Draw a bounding box around every leukocyte (white blood cell).
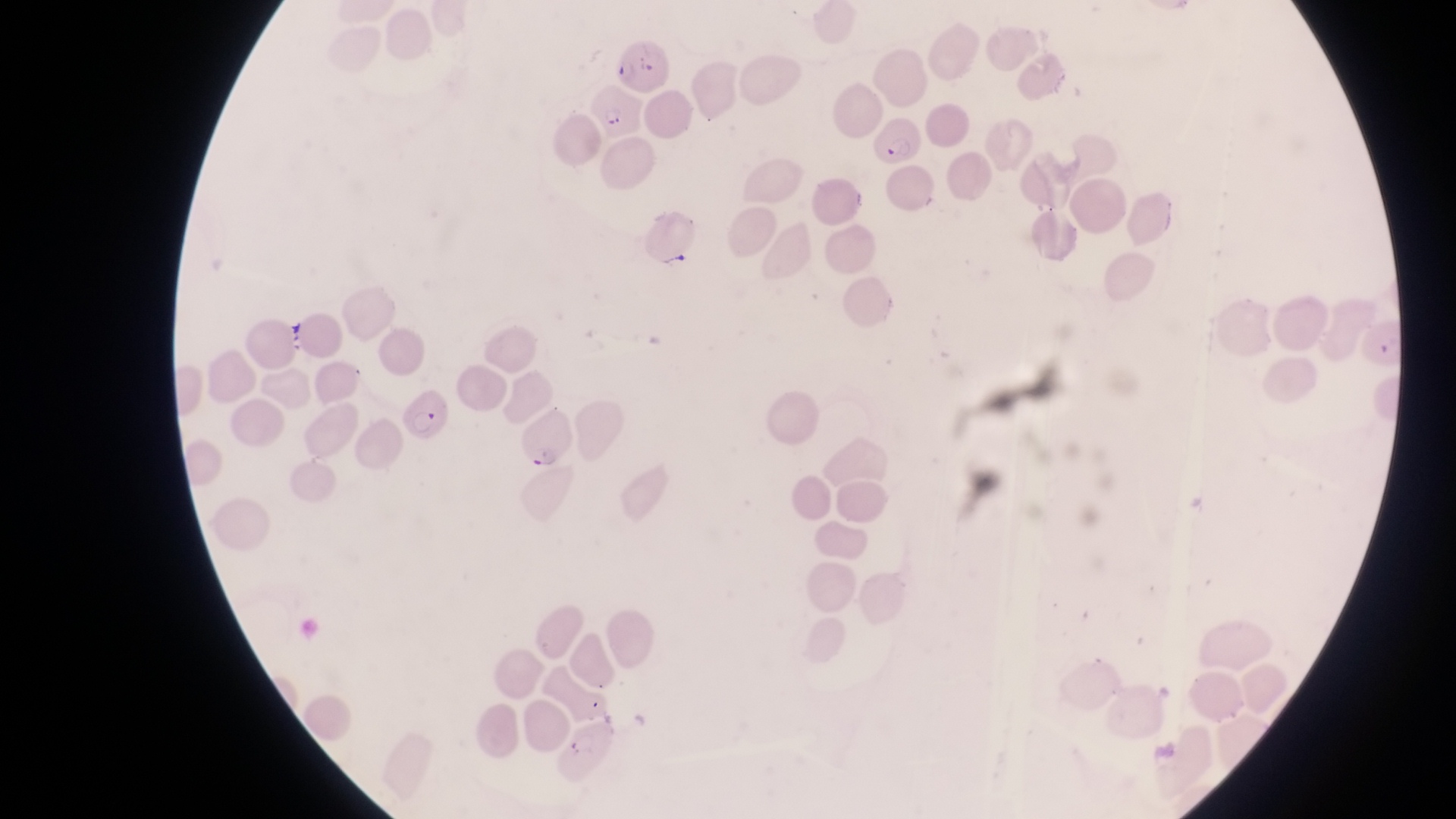
No leukocytes observed.

Approximate bounding boxes as left top right bottom in pixels.
Summary:
  - Parasitised red blood cell locations: 623 32 675 93; 592 82 642 140; 874 119 927 169; 403 391 450 449; 523 406 579 472
  - Artifact (platelet-like body, stain precipitate, or debris) locations: 661 249 693 276; 285 327 309 356
  - Country: Uganda
  - Preparation: thin blood film
  - Field of view: single
  - Magnification: 1000x
  - Image size: 1456×819 pixels
  - Capture: smartphone photograph through the eyepiece of an Olympus CX-23 microscope